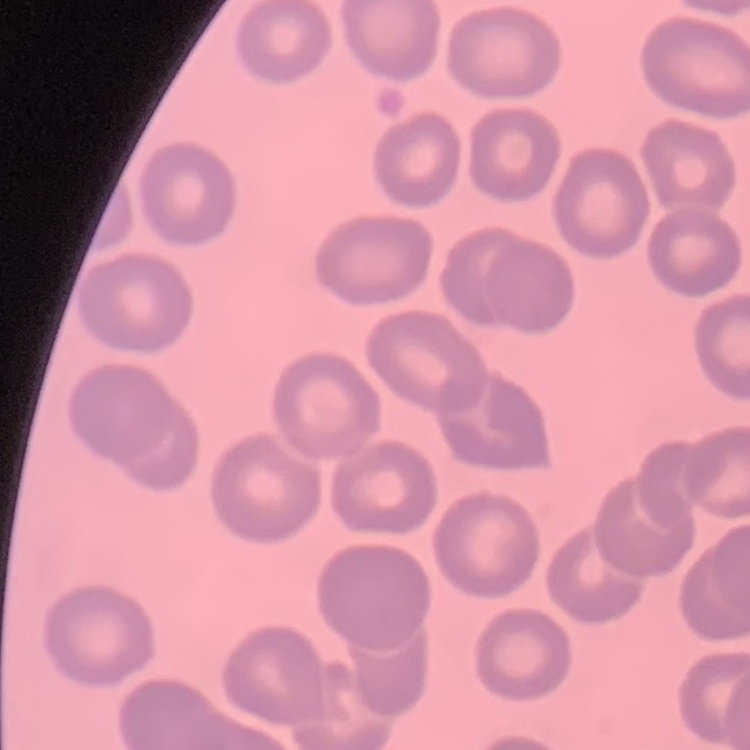

Summary:
  - Red blood cell morphology: no rouleaux formation
  - Stain: Field's or Giemsa
  - Preparation: thin blood smear
  - Image type: square crop of a larger photomicrograph